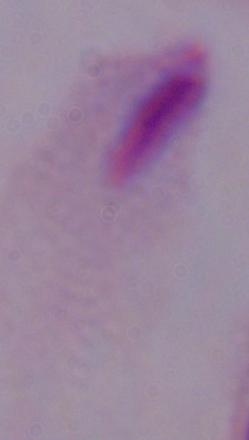
Summary:
  - Magnification: 1000x
  - Identification: trichomonad
  - Modality: micrograph